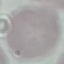
Summary:
  - Malaria status: uninfected
  - Image type: cell patch, automatically extracted from a larger field of view and resized to 64 × 64 pixels
  - Stain: Giemsa
  - Capture: smartphone camera at the microscope eyepiece
  - Preparation: thin smear